Assess this cell for malaria.
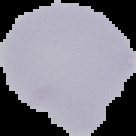

Uninfected.

image_size: 136×136 pixels
image_type: segmented cell region with the area outside set to black
preparation: thin blood smear